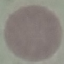

malaria_status: uninfected
stain: Giemsa
capture: smartphone camera at the microscope eyepiece
preparation: thin smear
image_type: cell patch, automatically extracted from a larger field of view and resized to 64 × 64 pixels